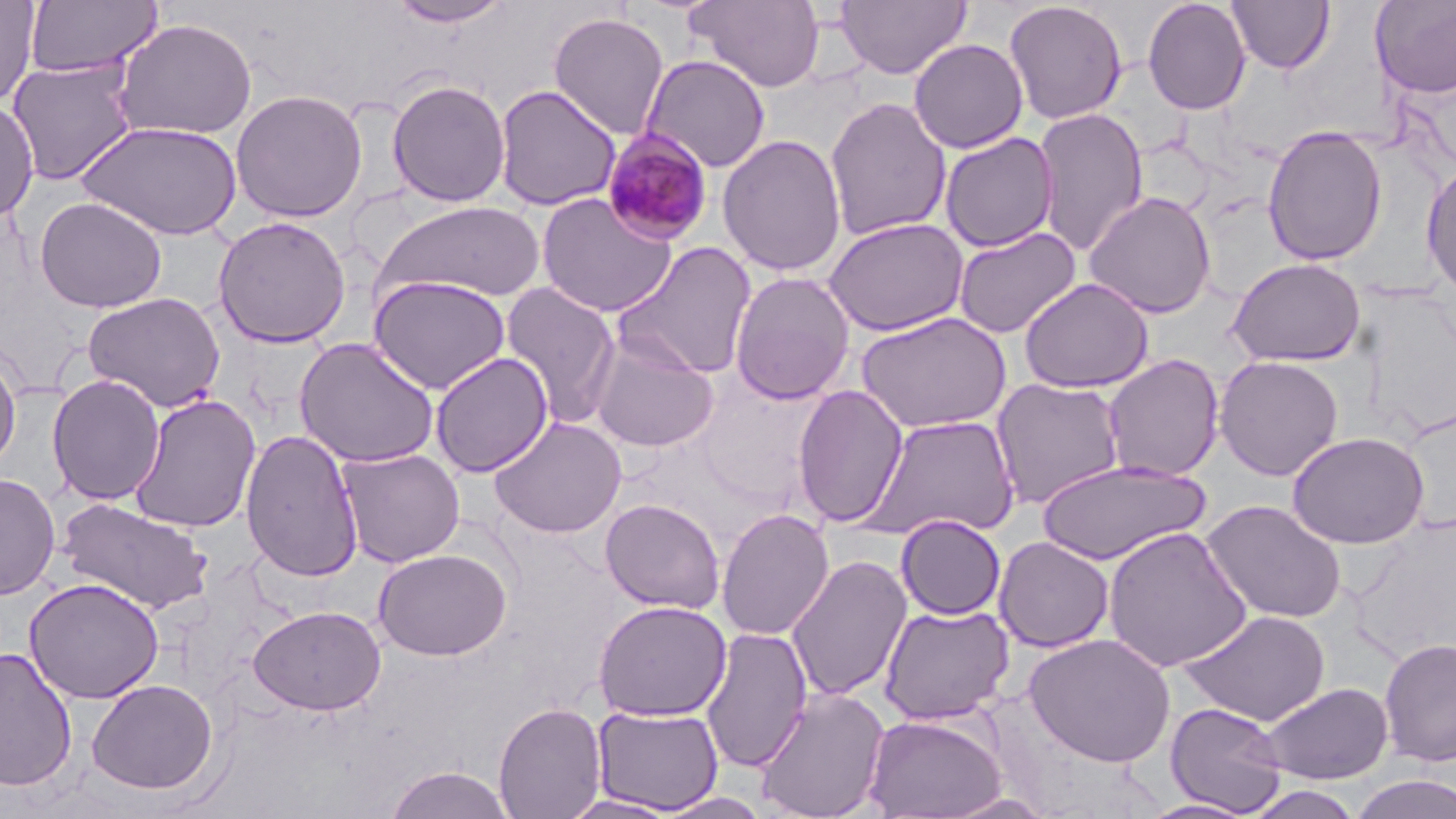

Summary:
  - Coordinate format: approximate bounding boxes as [x1, y1, x2, y2] in pixels
  - Plasmodium malariae-infected red blood cell locations: [601, 129, 715, 245]
  - Uninfected red blood cell locations: [0, 0, 40, 107], [24, 0, 162, 80], [387, 0, 515, 28], [686, 0, 826, 93], [835, 0, 971, 80], [1142, 0, 1252, 115], [1226, 0, 1335, 75], [1370, 0, 1456, 99], [1003, 1, 1128, 125], [548, 12, 669, 141], [111, 17, 258, 140], [909, 38, 1028, 153], [641, 55, 771, 173], [6, 58, 140, 185], [386, 79, 511, 207], [494, 85, 621, 212], [230, 89, 368, 222], [825, 96, 951, 241], [0, 99, 39, 224], [1033, 107, 1148, 258], [75, 119, 242, 241], [1262, 124, 1388, 266], [939, 131, 1059, 252], [717, 134, 847, 276], [1421, 161, 1456, 302], [1082, 190, 1217, 319], [535, 192, 678, 318], [34, 196, 167, 313], [371, 200, 547, 302], [212, 216, 351, 348], [823, 217, 969, 337], [952, 226, 1081, 338], [613, 242, 757, 379], [1226, 257, 1366, 367], [729, 271, 856, 404], [368, 275, 511, 395], [1020, 277, 1154, 393], [499, 283, 621, 427], [82, 291, 227, 413], [856, 311, 1012, 433], [588, 333, 721, 452], [294, 337, 441, 468], [0, 350, 21, 476], [429, 352, 553, 478], [1102, 354, 1224, 482], [1214, 355, 1344, 481], [46, 374, 166, 506], [991, 378, 1126, 509], [792, 383, 909, 528], [129, 394, 261, 533], [860, 414, 1020, 541], [488, 416, 627, 538], [241, 429, 364, 582], [1287, 431, 1429, 549], [336, 447, 465, 567], [1034, 460, 1211, 565], [0, 473, 60, 600], [55, 498, 214, 615], [600, 498, 725, 614], [1201, 499, 1347, 624], [716, 508, 834, 640], [895, 515, 1006, 620], [1103, 526, 1253, 673], [994, 536, 1114, 653], [372, 547, 512, 661], [786, 554, 912, 702], [24, 577, 165, 704], [593, 600, 731, 721], [878, 603, 1014, 725], [248, 605, 386, 716], [1179, 610, 1331, 727], [700, 627, 812, 773], [1024, 633, 1176, 767], [1379, 636, 1456, 768], [0, 647, 78, 792], [87, 678, 218, 795], [1260, 681, 1394, 784], [755, 686, 891, 819], [494, 701, 607, 818], [1165, 701, 1288, 815], [592, 704, 724, 814], [862, 713, 1009, 818], [383, 765, 516, 819], [1349, 774, 1456, 819], [653, 791, 773, 819], [559, 794, 683, 818], [1137, 798, 1259, 818]
  - Slide-level diagnosis: Plasmodium malariae
  - Image size: 1456×819 pixels
  - Magnification: 1000x
  - Modality: light microscopy
  - Preparation: thin blood smear
  - Stain: May-Grünwald-Giemsa
  - Field of view: single